Give the position of every Plasmodium parasite visible.
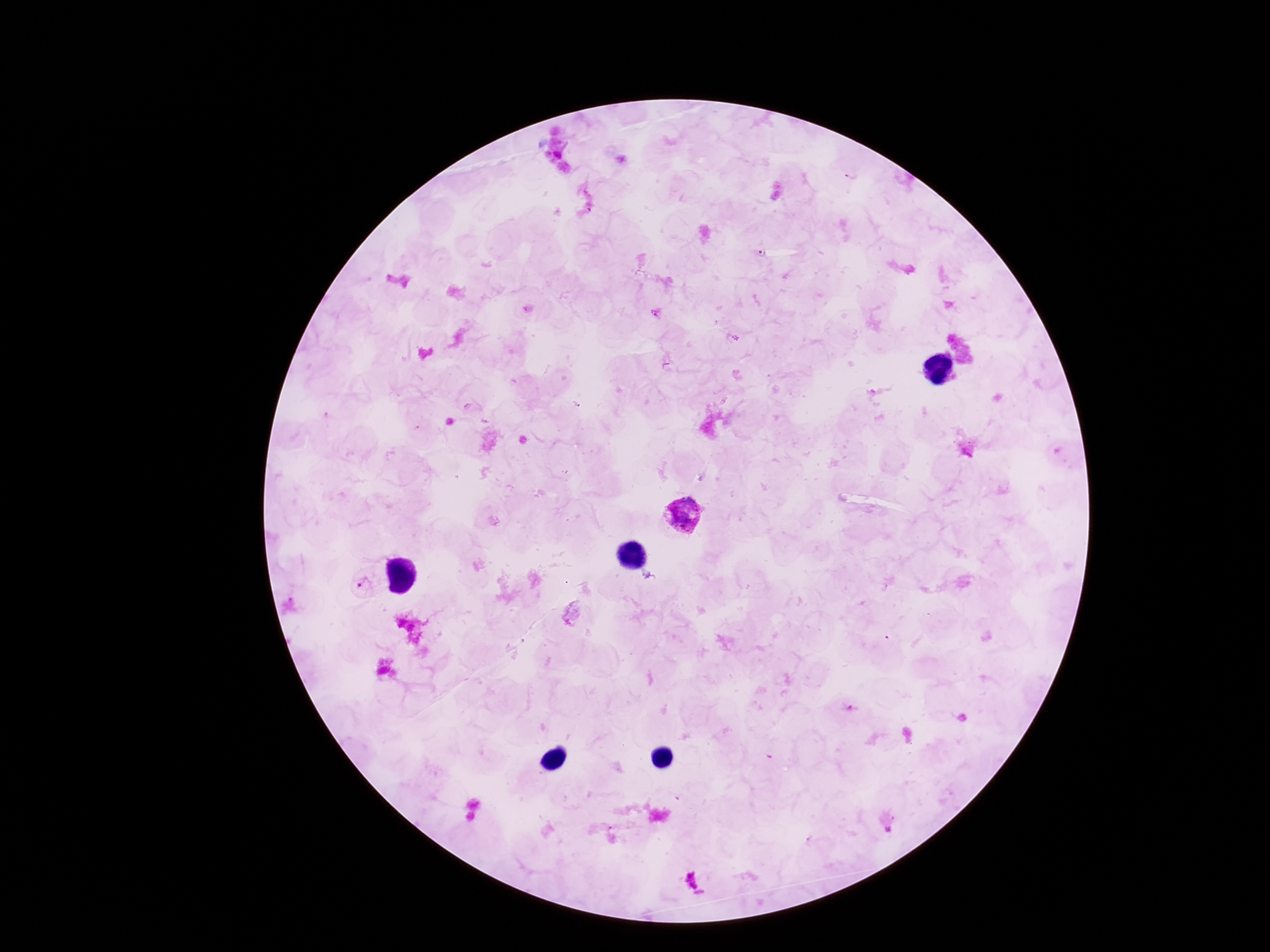
Approximate centers as (x, y) in pixels.
Plasmodium parasites: (682, 516), (364, 585), (689, 879).

magnification = 100x
patient malaria status = infected
image size = 1270×952 pixels
preparation = thick peripheral-blood smear
stain = Giemsa
field of view = single
capture = smartphone camera through the microscope eyepiece